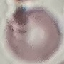

Malaria status: uninfected. Giemsa-stained preparation. Acquired by smartphone through the microscope eyepiece. Thin smear of blood. Automatically extracted cell patch, resized to 64 × 64 pixels.